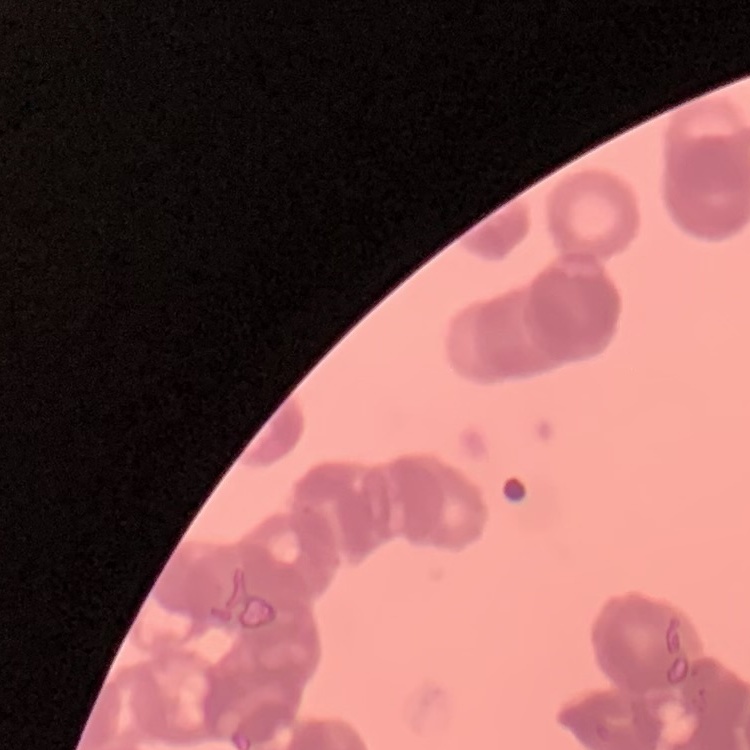
Summary:
  - Red blood cell morphology: rouleaux formation
  - Image type: one tile cut from a larger photomicrograph
  - Stain: Field's or Giemsa
  - Preparation: thin peripheral smear